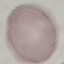

result = no malaria parasites seen
preparation = thin blood smear
capture = smartphone through the microscope eyepiece
stain = Giemsa
image type = cell patch, automatically extracted from a larger field of view and resized to 64 × 64 pixels